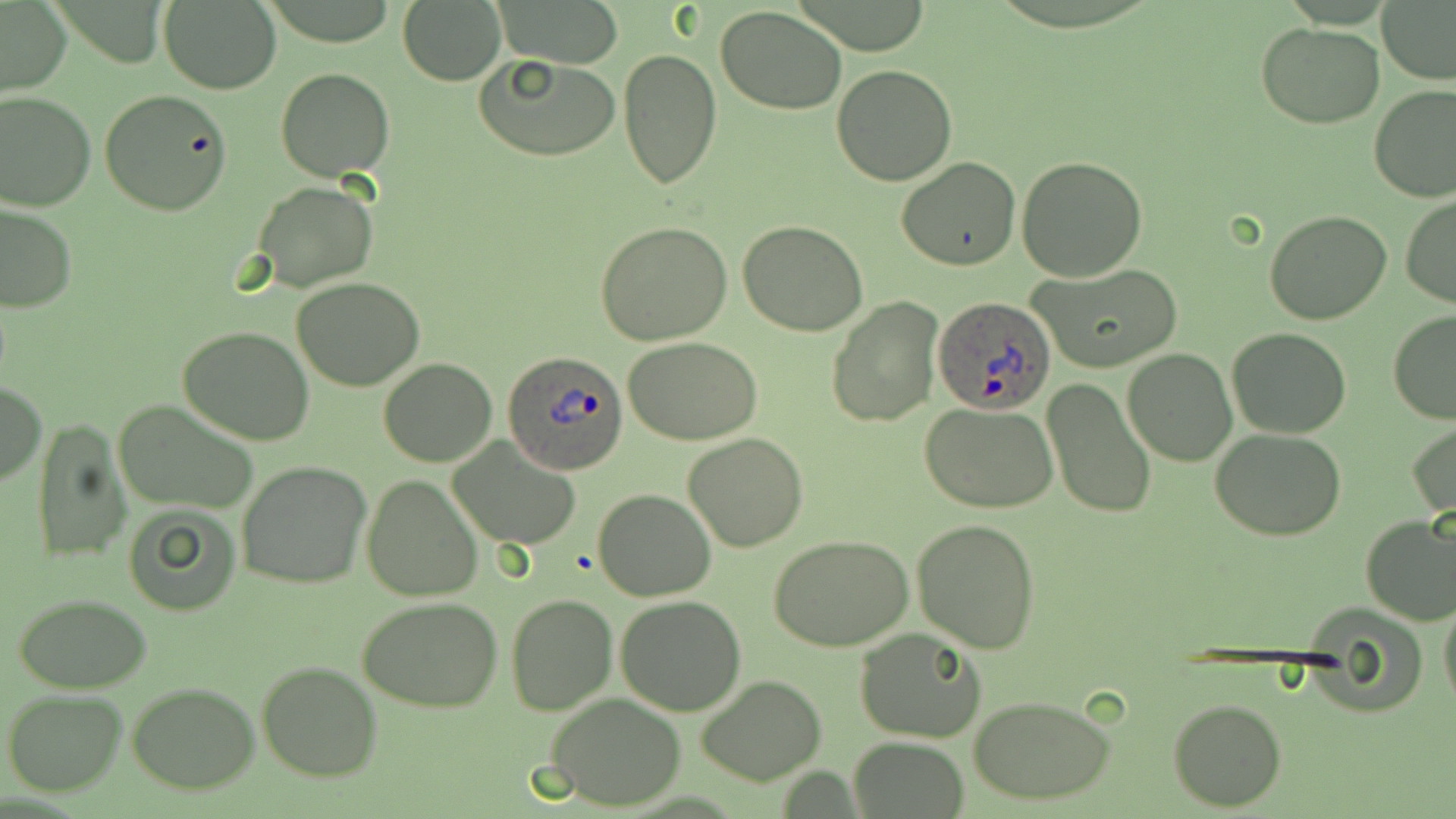 Approximate bounding boxes as named x1/y1/x2/y2 corners in pixels. Uninfected red blood cell locations: (x1=498, y1=0, x2=624, y2=68), (x1=159, y1=1, x2=282, y2=94), (x1=398, y1=2, x2=505, y2=84), (x1=1380, y1=2, x2=1456, y2=85), (x1=0, y1=3, x2=72, y2=94), (x1=716, y1=5, x2=847, y2=116), (x1=1256, y1=21, x2=1384, y2=128), (x1=618, y1=49, x2=721, y2=190), (x1=473, y1=52, x2=620, y2=162), (x1=831, y1=64, x2=959, y2=186), (x1=276, y1=69, x2=395, y2=180), (x1=1370, y1=85, x2=1456, y2=203), (x1=0, y1=88, x2=96, y2=211), (x1=99, y1=90, x2=233, y2=215), (x1=1016, y1=156, x2=1148, y2=281), (x1=896, y1=158, x2=1023, y2=271), (x1=252, y1=180, x2=378, y2=293), (x1=1401, y1=195, x2=1456, y2=307), (x1=0, y1=202, x2=77, y2=312), (x1=1264, y1=209, x2=1394, y2=326), (x1=737, y1=220, x2=868, y2=337), (x1=594, y1=222, x2=734, y2=346), (x1=1030, y1=264, x2=1184, y2=374), (x1=292, y1=275, x2=424, y2=390), (x1=827, y1=297, x2=941, y2=427), (x1=1387, y1=311, x2=1456, y2=424), (x1=178, y1=324, x2=316, y2=446), (x1=1228, y1=326, x2=1350, y2=439), (x1=621, y1=335, x2=763, y2=445), (x1=1122, y1=348, x2=1237, y2=466), (x1=378, y1=358, x2=498, y2=467), (x1=1042, y1=378, x2=1158, y2=522), (x1=1, y1=382, x2=47, y2=484), (x1=113, y1=399, x2=260, y2=516), (x1=921, y1=400, x2=1058, y2=514), (x1=31, y1=417, x2=131, y2=562), (x1=1407, y1=421, x2=1455, y2=520), (x1=1210, y1=429, x2=1349, y2=541), (x1=683, y1=433, x2=809, y2=552), (x1=447, y1=437, x2=582, y2=551), (x1=235, y1=460, x2=373, y2=590), (x1=361, y1=475, x2=484, y2=603), (x1=593, y1=490, x2=716, y2=601), (x1=122, y1=502, x2=243, y2=617), (x1=1360, y1=512, x2=1456, y2=625), (x1=912, y1=518, x2=1041, y2=654), (x1=769, y1=534, x2=917, y2=652), (x1=1440, y1=593, x2=1456, y2=709), (x1=506, y1=594, x2=617, y2=715), (x1=14, y1=595, x2=153, y2=692), (x1=616, y1=598, x2=747, y2=715), (x1=358, y1=599, x2=502, y2=713), (x1=854, y1=629, x2=987, y2=744), (x1=257, y1=661, x2=383, y2=781), (x1=695, y1=675, x2=825, y2=786), (x1=127, y1=682, x2=260, y2=795), (x1=3, y1=690, x2=128, y2=796), (x1=543, y1=692, x2=689, y2=811), (x1=970, y1=696, x2=1117, y2=805), (x1=1168, y1=697, x2=1287, y2=811), (x1=849, y1=736, x2=970, y2=817). Plasmodium ovale-infected red blood cell locations: (x1=932, y1=297, x2=1056, y2=413), (x1=505, y1=352, x2=627, y2=474). Slide-level diagnosis: Plasmodium ovale. Single field of view. Optical microscopy. 1000x magnification. May-Grünwald-Giemsa-stained preparation. Thin blood smear. Image is 1456×819 pixels.